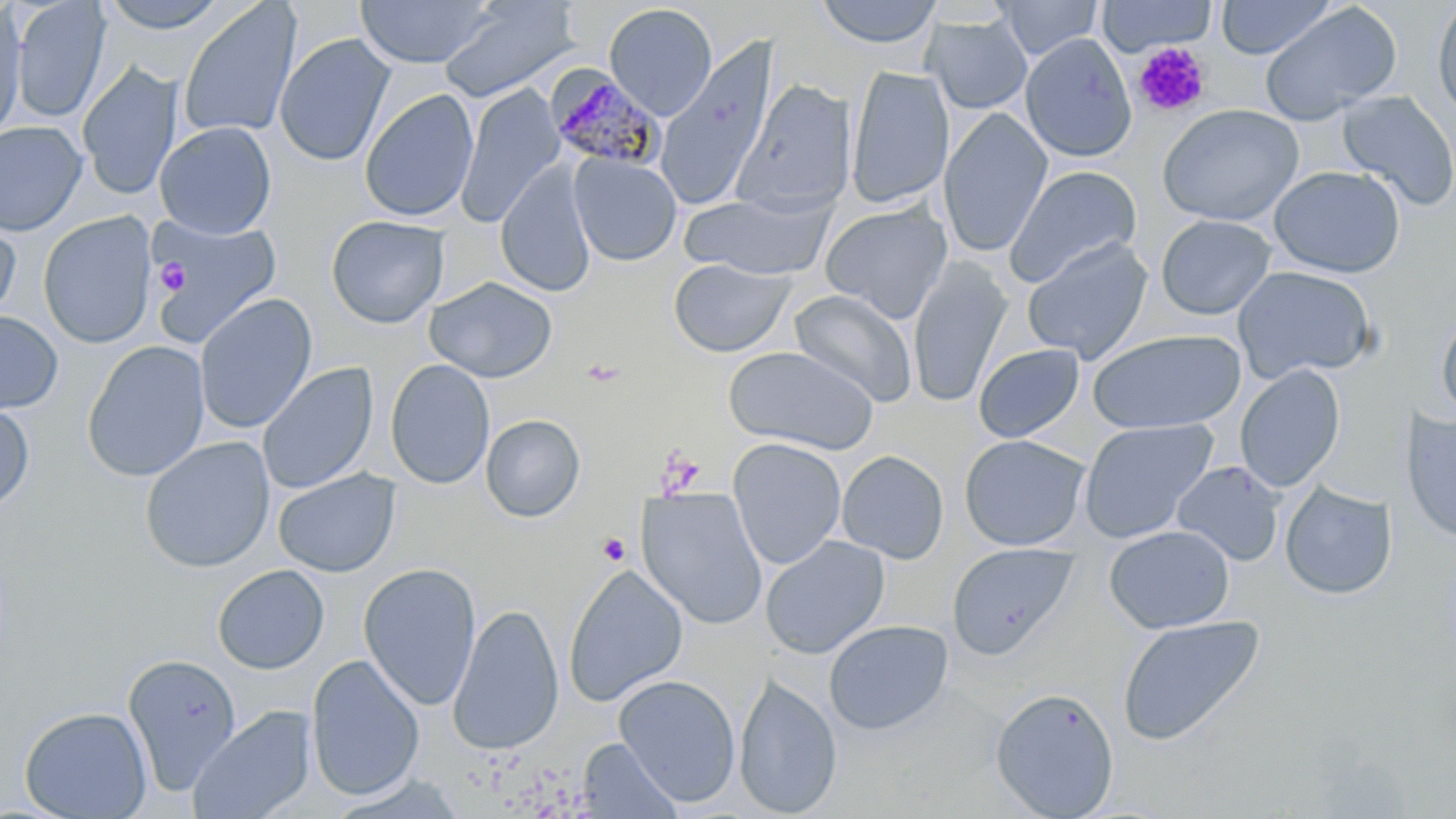
{
  "slide_level_diagnosis": "Plasmodium malariae",
  "stain": "May-Grünwald-Giemsa",
  "modality": "light microscopy",
  "plasmodium_malariae_infected_red_blood_cell_locations": "approximate bounding boxes as named x1/y1/x2/y2 corners in pixels: (x1=545, y1=65, x2=667, y2=171)",
  "platelet_locations": "approximate bounding boxes as named x1/y1/x2/y2 corners in pixels: (x1=1133, y1=41, x2=1210, y2=117), (x1=155, y1=259, x2=188, y2=294), (x1=655, y1=449, x2=704, y2=497), (x1=597, y1=533, x2=631, y2=566)",
  "magnification": "1000x",
  "field_of_view": "single",
  "image_size": "1456×819 pixels",
  "uninfected_red_blood_cell_locations": "approximate bounding boxes as named x1/y1/x2/y2 corners in pixels: (x1=11, y1=0, x2=111, y2=122), (x1=98, y1=0, x2=229, y2=33), (x1=355, y1=0, x2=495, y2=68), (x1=438, y1=0, x2=578, y2=103), (x1=817, y1=0, x2=942, y2=49), (x1=995, y1=0, x2=1103, y2=60), (x1=1098, y1=0, x2=1215, y2=56), (x1=1216, y1=0, x2=1338, y2=59), (x1=0, y1=1, x2=27, y2=143), (x1=177, y1=1, x2=301, y2=142), (x1=1259, y1=2, x2=1402, y2=126), (x1=1430, y1=2, x2=1456, y2=119), (x1=603, y1=3, x2=718, y2=119), (x1=923, y1=15, x2=1033, y2=115), (x1=274, y1=32, x2=394, y2=168), (x1=1020, y1=33, x2=1137, y2=162), (x1=655, y1=36, x2=781, y2=211), (x1=1133, y1=44, x2=1213, y2=117), (x1=77, y1=62, x2=182, y2=201), (x1=845, y1=65, x2=954, y2=210), (x1=733, y1=79, x2=857, y2=214), (x1=457, y1=83, x2=565, y2=228), (x1=360, y1=88, x2=478, y2=223), (x1=1337, y1=90, x2=1456, y2=211), (x1=1157, y1=104, x2=1305, y2=226), (x1=938, y1=108, x2=1052, y2=258), (x1=0, y1=121, x2=87, y2=236), (x1=154, y1=121, x2=276, y2=239), (x1=569, y1=153, x2=681, y2=266), (x1=495, y1=162, x2=598, y2=298), (x1=1005, y1=165, x2=1141, y2=287), (x1=1269, y1=165, x2=1405, y2=278), (x1=680, y1=190, x2=836, y2=279), (x1=819, y1=202, x2=953, y2=323), (x1=38, y1=211, x2=157, y2=348), (x1=0, y1=213, x2=21, y2=326), (x1=147, y1=213, x2=282, y2=347), (x1=325, y1=214, x2=449, y2=328), (x1=1156, y1=214, x2=1277, y2=320), (x1=1021, y1=237, x2=1153, y2=364), (x1=668, y1=257, x2=794, y2=357), (x1=907, y1=258, x2=1012, y2=408), (x1=1232, y1=266, x2=1378, y2=383), (x1=424, y1=276, x2=557, y2=383), (x1=789, y1=289, x2=918, y2=407), (x1=194, y1=293, x2=317, y2=434), (x1=0, y1=310, x2=63, y2=413), (x1=1435, y1=310, x2=1456, y2=424), (x1=1088, y1=329, x2=1247, y2=434), (x1=82, y1=340, x2=210, y2=482), (x1=973, y1=343, x2=1085, y2=443), (x1=722, y1=345, x2=880, y2=454), (x1=385, y1=358, x2=496, y2=490), (x1=257, y1=361, x2=378, y2=496), (x1=1234, y1=364, x2=1346, y2=493), (x1=0, y1=399, x2=35, y2=514), (x1=1400, y1=410, x2=1456, y2=545), (x1=481, y1=414, x2=586, y2=522), (x1=1078, y1=418, x2=1219, y2=543), (x1=959, y1=434, x2=1089, y2=551), (x1=139, y1=436, x2=275, y2=573), (x1=727, y1=437, x2=847, y2=570), (x1=836, y1=450, x2=949, y2=563), (x1=1172, y1=461, x2=1286, y2=566), (x1=273, y1=468, x2=400, y2=578), (x1=1280, y1=481, x2=1397, y2=600), (x1=637, y1=488, x2=769, y2=630), (x1=1104, y1=525, x2=1235, y2=633), (x1=760, y1=535, x2=890, y2=659), (x1=947, y1=542, x2=1077, y2=658), (x1=358, y1=563, x2=482, y2=710), (x1=212, y1=564, x2=329, y2=674), (x1=564, y1=565, x2=687, y2=706), (x1=447, y1=602, x2=565, y2=755), (x1=1116, y1=614, x2=1265, y2=746), (x1=823, y1=619, x2=954, y2=735), (x1=122, y1=653, x2=242, y2=794), (x1=306, y1=654, x2=425, y2=801), (x1=734, y1=673, x2=843, y2=817), (x1=614, y1=674, x2=741, y2=806), (x1=990, y1=687, x2=1119, y2=818), (x1=187, y1=705, x2=316, y2=819), (x1=19, y1=706, x2=152, y2=819), (x1=576, y1=738, x2=682, y2=819)",
  "preparation": "thin blood film"
}